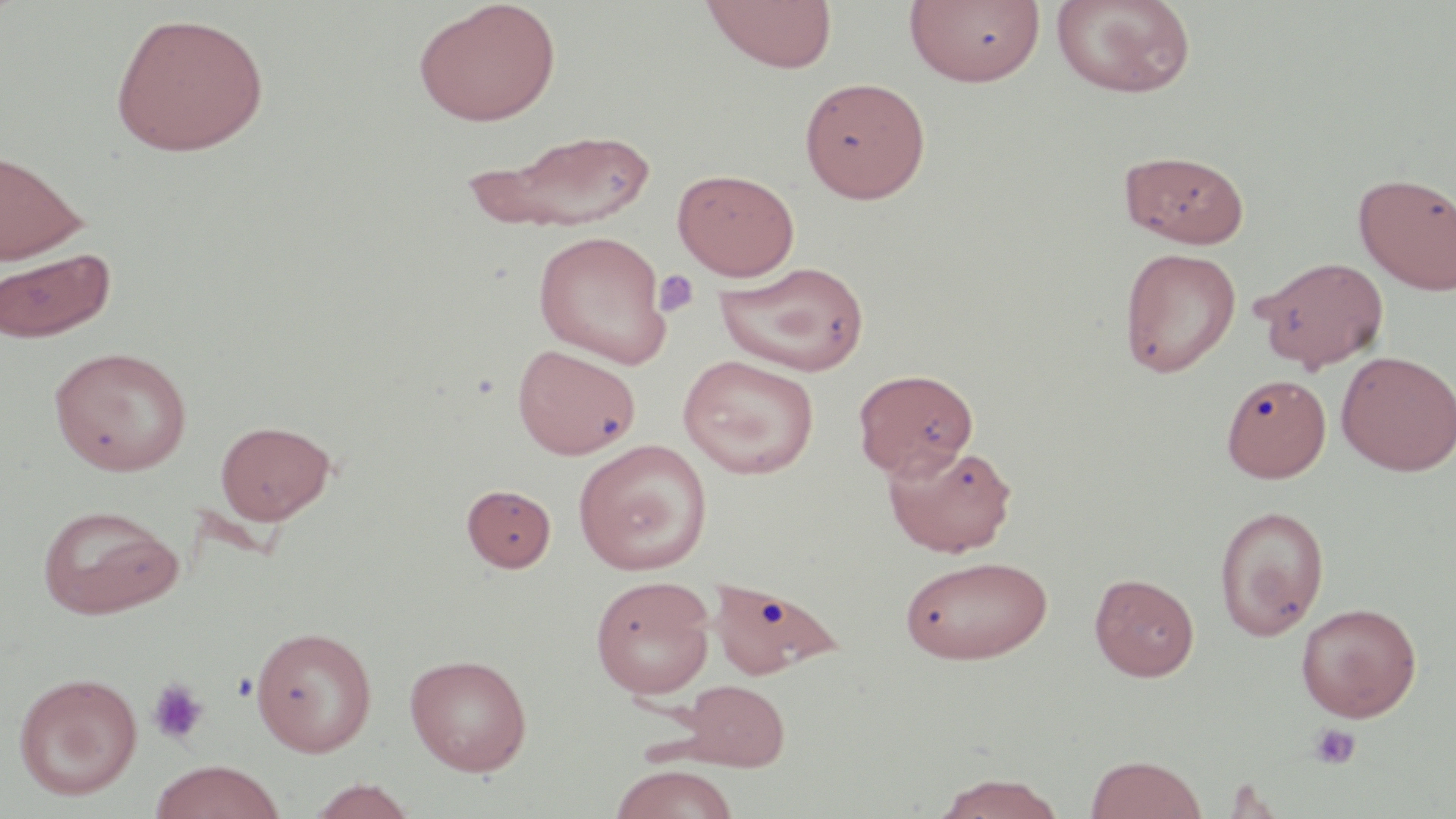

Summary:
  - Coordinate format: approximate bounding boxes as (x1,y1)-(x2,y2) corner pairs in pixels
  - Platelet locations: (653,269)-(699,317), (146,679)-(210,746), (1309,723)-(1362,769)
  - Uninfected red blood cell locations: (700,0)-(838,73), (904,0)-(1047,88), (1051,0)-(1196,98), (413,1)-(562,126), (109,10)-(270,157), (799,76)-(931,203), (468,127)-(660,232), (0,148)-(88,265), (1119,150)-(1250,248), (672,168)-(799,280), (1354,172)-(1456,294), (533,230)-(672,368), (1,247)-(116,344), (1118,247)-(1241,377), (1253,255)-(1390,371), (714,261)-(870,376), (512,343)-(642,460), (49,345)-(192,476), (1336,350)-(1456,475), (678,354)-(821,479), (853,368)-(978,478), (1222,372)-(1331,482), (215,419)-(335,525), (572,439)-(712,575), (883,442)-(1018,557), (461,483)-(556,572), (37,504)-(182,619), (1213,504)-(1330,640), (899,553)-(1053,665), (1089,572)-(1199,681), (590,575)-(716,699), (708,575)-(843,681), (1296,602)-(1422,721), (251,625)-(377,756), (404,653)-(533,776), (13,671)-(143,800), (680,679)-(789,771), (1084,754)-(1207,819), (150,759)-(287,819), (608,763)-(739,819), (931,772)-(1069,818), (306,779)-(419,819)
  - Slide-level diagnosis: negative for blood parasites
  - Modality: optical microscopy
  - Stain: May-Grünwald-Giemsa
  - Image size: 1456×819 pixels
  - Preparation: thin blood smear
  - Field of view: one of a larger specimen
  - Magnification: 1000x